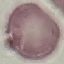
Malaria status: uninfected. Thin blood film. Giemsa stain. Photographed with a smartphone camera at the microscope eyepiece. Automatically extracted cell patch, resized to 64 × 64 pixels.